Report the malaria status of this cell.
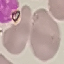
Uninfected.

Summary:
  - Image type: cell patch, automatically extracted from a larger field of view and resized to 64 × 64 pixels
  - Preparation: thin blood film
  - Stain: Giemsa
  - Capture: smartphone camera at the microscope eyepiece